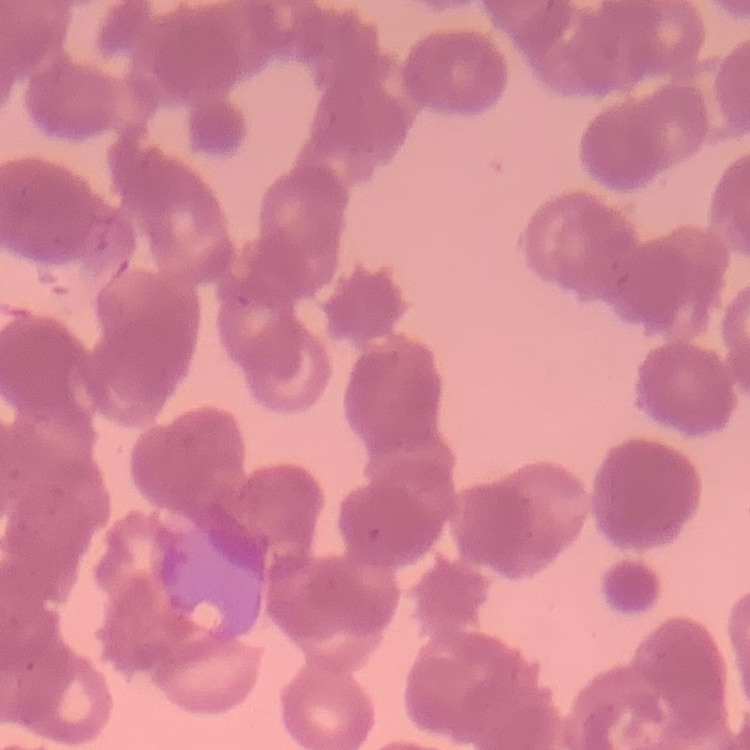
The red blood cells show rouleaux formation. Square crop of a larger photomicrograph. Stained with either Field's or Giemsa. Thin blood smear.